Name the parasite shown.
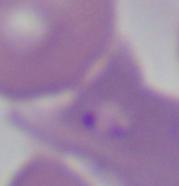

Babesia.

Summary:
  - Magnification: 1000x
  - Modality: photomicrograph